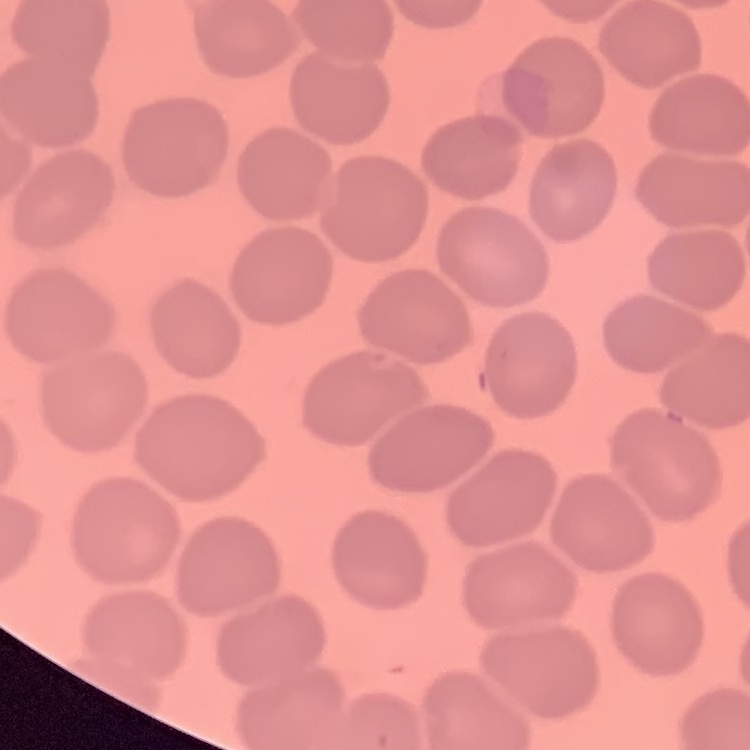
{
  "erythrocyte_morphology": "no rouleaux formation",
  "stain": "Field's or Giemsa",
  "preparation": "thin blood smear",
  "image_type": "square crop of a larger photomicrograph"
}